Point out each malaria parasite.
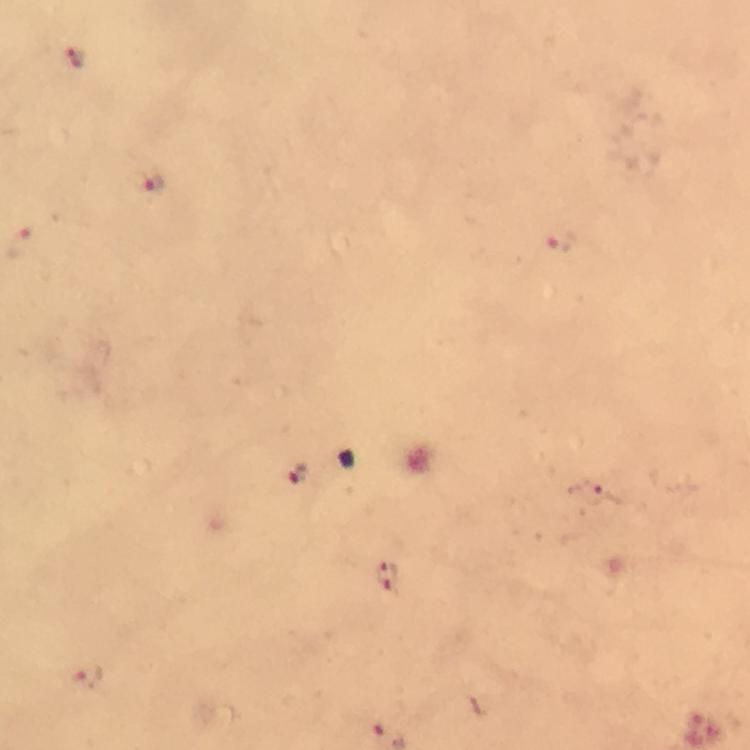
Approximate centers as [x, y] in pixels.
Malaria parasites: [74, 59], [154, 185], [560, 239], [23, 244], [299, 474], [595, 491], [387, 577], [88, 676].

Summary:
  - Cropped from: one field of view
  - Context: from a malaria diagnostic workup
  - Preparation: thick blood film
  - Stain: Giemsa
  - Capture: smartphone photograph through a microscope
  - Immersion oil: used
  - Magnification: 100x
  - Image size: 750×750 pixels